Outline each blood parasite and name the species.
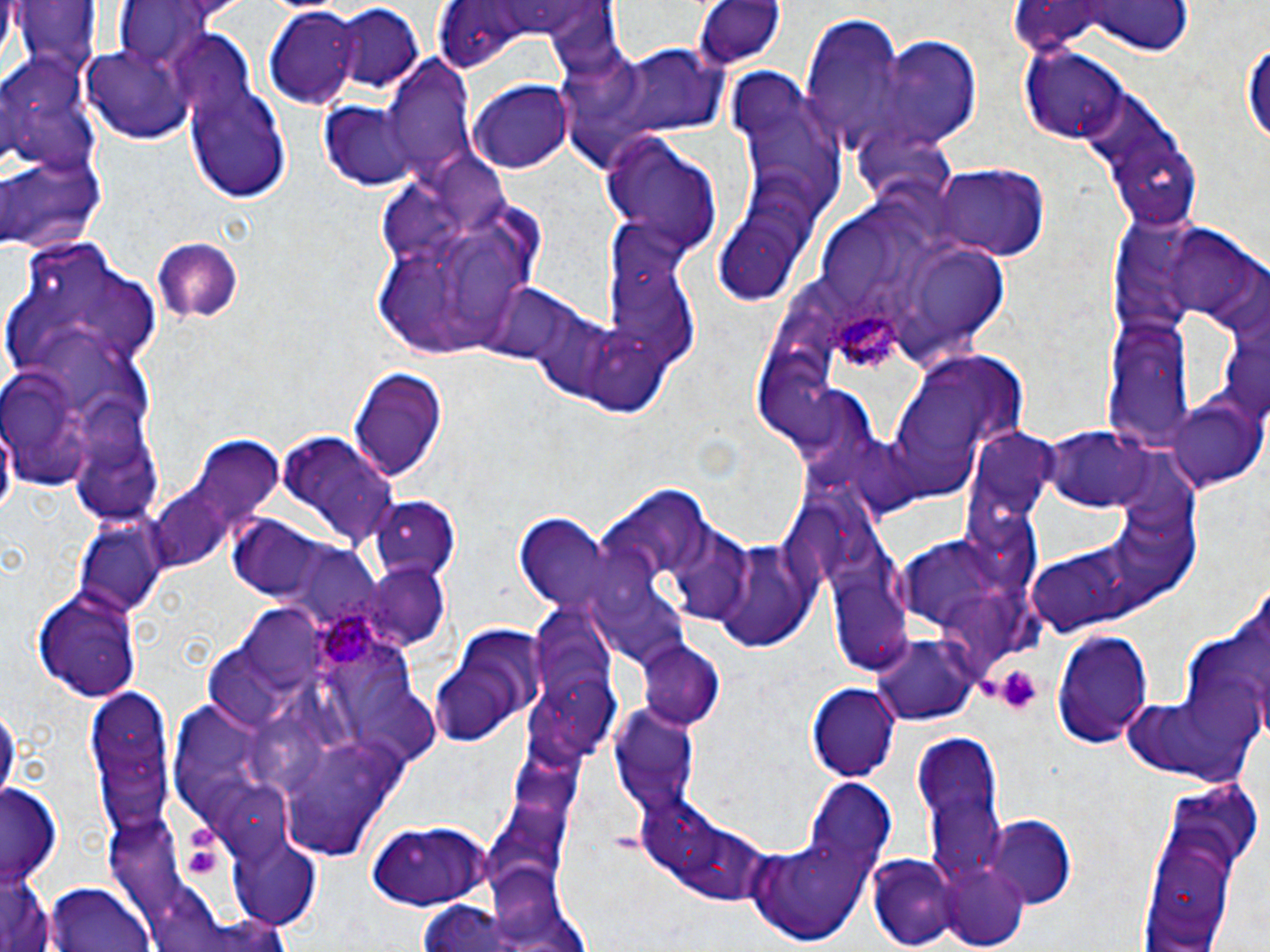
Approximate bounding boxes as (x1,y1)-(x2,y2) corner pairs in pixels.
Plasmodium ovale-infected red blood cells: (826,298)-(908,376), (305,596)-(408,686).
No Plasmodium falciparum, Plasmodium malariae, Plasmodium vivax, Babesia divergens, or Trypanosoma brucei observed.

{
  "slide_level_diagnosis": "Plasmodium ovale",
  "preparation": "thin blood film",
  "field_of_view": "single",
  "magnification": "1000x",
  "uninfected_red_blood_cell_locations": "approximate bounding boxes as (x1,y1)-(x2,y2) corner pairs in pixels: (1082,0)-(1196,58), (693,1)-(783,70), (103,2)-(234,70), (11,3)-(102,84), (427,3)-(622,77), (331,5)-(423,91), (264,7)-(361,112), (801,13)-(910,148), (1239,27)-(1270,156), (555,35)-(732,166), (874,37)-(982,149), (83,41)-(197,146), (1023,46)-(1127,140), (377,53)-(481,183), (1,55)-(100,174), (728,69)-(815,138), (469,80)-(572,174), (186,83)-(293,204), (316,102)-(417,191), (600,132)-(728,260), (1114,141)-(1201,223), (0,147)-(107,254), (927,163)-(1051,260), (364,194)-(551,364), (600,213)-(707,380), (820,217)-(900,299), (719,225)-(793,302), (1164,227)-(1265,326), (151,236)-(243,323), (6,237)-(165,387), (917,253)-(1002,340), (481,280)-(588,368), (1105,320)-(1197,452), (888,346)-(1023,480), (1,359)-(90,488), (755,362)-(841,451), (347,365)-(451,482), (1170,395)-(1265,491), (71,418)-(167,527), (1043,423)-(1164,511), (965,426)-(1062,544), (277,431)-(398,548), (197,433)-(287,517), (370,495)-(463,580), (887,513)-(1050,674), (515,515)-(617,613), (75,523)-(167,614), (710,535)-(817,653), (1033,560)-(1103,628), (361,565)-(450,652), (829,580)-(913,677), (35,585)-(142,705), (243,609)-(320,692), (431,617)-(556,738), (1052,629)-(1155,745), (872,634)-(979,726), (637,642)-(723,730), (1114,660)-(1268,791), (555,675)-(612,760), (804,680)-(901,784), (88,687)-(176,846), (0,700)-(19,806), (178,702)-(254,771), (609,704)-(700,822), (248,717)-(330,797), (914,735)-(1007,891), (288,757)-(369,861), (806,778)-(900,870), (215,780)-(289,870), (1,784)-(62,889), (632,790)-(775,906), (1140,796)-(1254,952), (742,811)-(886,947), (987,812)-(1077,907), (365,818)-(495,911), (228,837)-(324,931), (868,852)-(956,952), (941,861)-(1027,948), (3,862)-(57,952), (487,868)-(575,945), (46,883)-(155,952), (414,900)-(515,952)",
  "stain": "May-Grünwald-Giemsa",
  "platelet_locations": "approximate bounding boxes as (x1,y1)-(x2,y2) corner pairs in pixels: (998,666)-(1041,714), (188,821)-(216,848), (187,851)-(220,877)",
  "image_size": "1270×952 pixels",
  "modality": "light microscopy"
}